State which cell type is depicted.
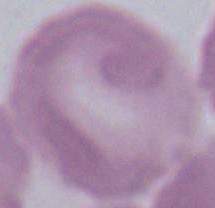

This is an erythrocyte.

Micrograph. Captured at 1000x magnification.